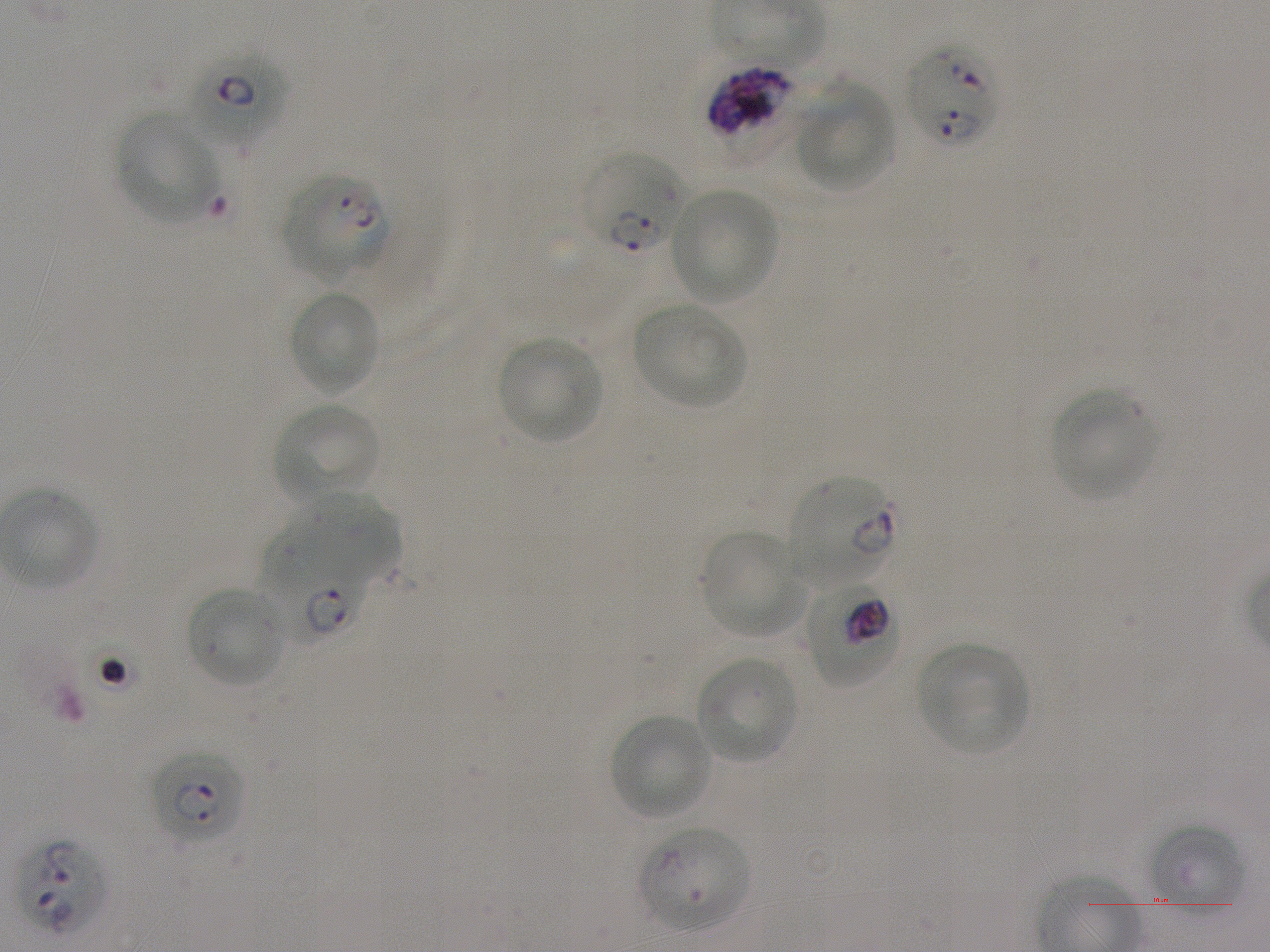
Not every red blood cell is marked. A life-cycle stage — or a range of stages, where the recorded stages span more than one — follows each staged infected red blood cell.
{
  "preparation": "thin blood smear",
  "life_cycle_stages_observed": "ring, trophozoite",
  "locations_of_infected_red_blood_cells": "approximate bounding boxes as {x1, y1, x2, y2} in pixels: {906, 42, 1000, 149}; {182, 44, 288, 147} early ring to early trophozoite; {705, 64, 794, 139}; {580, 152, 684, 255} ring; {280, 172, 389, 280} ring; {786, 476, 897, 587} early ring to early trophozoite; {262, 525, 367, 644} early ring to early trophozoite; {805, 581, 900, 688} trophozoite; {149, 749, 245, 847} ring; {639, 826, 751, 932} ring; {17, 837, 110, 937}",
  "objective": "100x, oil immersion, numerical aperture 1.25",
  "image_size": "1270×952 pixels",
  "donor_blood_group": "A+",
  "culture": "static in-vitro P. falciparum strain NF54",
  "field_of_view": "single",
  "stain": "Giemsa",
  "locations_of_uninfected_red_blood_cells": "approximate bounding boxes as {x1, y1, x2, y2} in pixels: {796, 83, 896, 191}, {116, 111, 218, 224}, {670, 188, 779, 303}, {287, 290, 382, 396}, {633, 303, 748, 408}, {497, 336, 603, 444}, {1050, 390, 1157, 501}, {272, 402, 382, 504}, {2, 487, 100, 591}, {290, 499, 402, 581}, {699, 531, 805, 637}, {185, 585, 287, 689}, {917, 643, 1031, 755}, {695, 656, 799, 765}, {609, 714, 712, 820}, {1152, 824, 1245, 914}"
}